Report the malaria status of this cell.
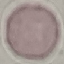

Uninfected.

{
  "stain": "Giemsa",
  "preparation": "thin smear",
  "capture": "smartphone through the microscope eyepiece",
  "image_type": "cell patch, automatically extracted from a larger field of view and resized to 64 × 64 pixels"
}